Assess this cell for malaria.
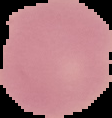
Uninfected.

preparation: thin blood smear
image_type: segmented cell region on a black background
image_size: 112×118 pixels